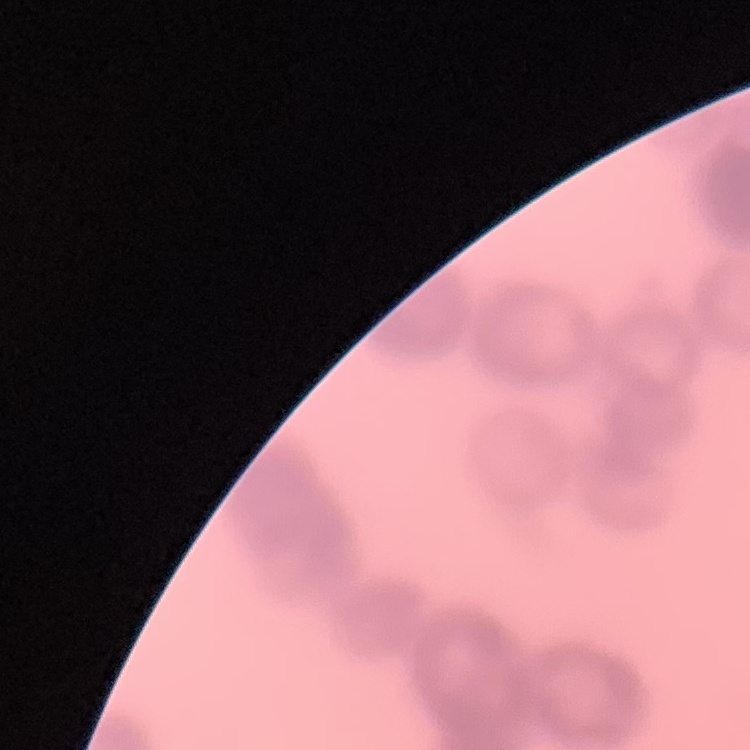

Summary:
  - Erythrocyte morphology: rouleaux formation
  - Stain: Field's or Giemsa
  - Image type: square crop of a larger photomicrograph
  - Preparation: thin blood smear